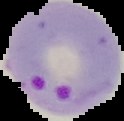

From a thin blood film. Cell region segmented out of the field of view; the surrounding area is masked to black. Result: Plasmodium parasites detected. Image is 124×121 pixels.